Classify this cell by malaria status.
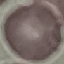
It is uninfected.

Giemsa stain. Acquired by smartphone through the microscope eyepiece. Cell patch, automatically extracted from a larger field of view and resized to 64 × 64 pixels. Thin blood smear.